Describe the morphology of the erythrocytes.
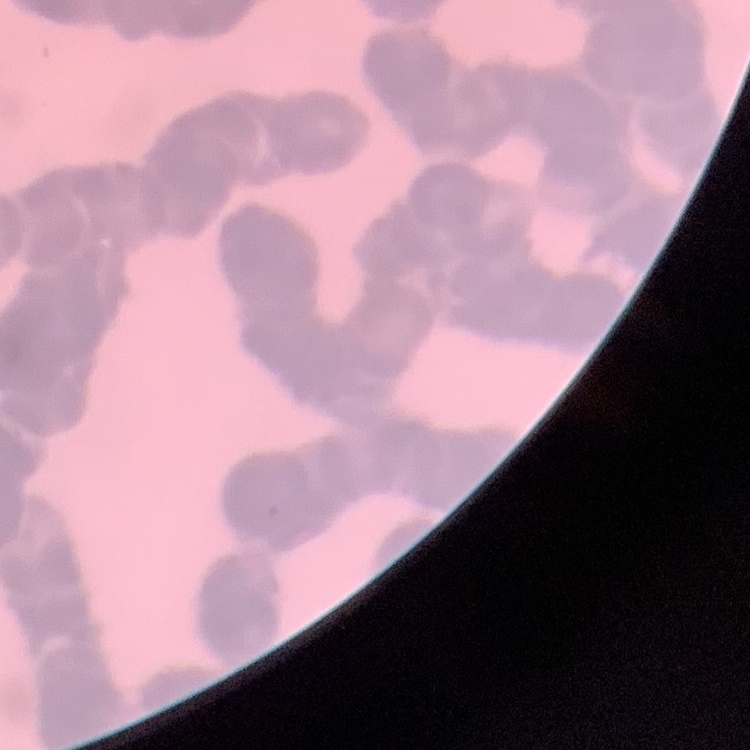
Rouleaux formation.

stain = Field's or Giemsa
preparation = thin blood smear
image type = one tile cut from a larger photomicrograph